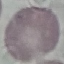 Result: no malaria parasites detected. Automatically extracted cell patch, resized to 64 × 64 pixels. Photographed with a smartphone camera at the microscope eyepiece. Giemsa stain. Thin blood smear.